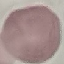

Malaria status: uninfected. Giemsa stain. Thin smear of blood. Acquired by smartphone through the microscope eyepiece. Automatically extracted cell patch, resized to 64 × 64 pixels.